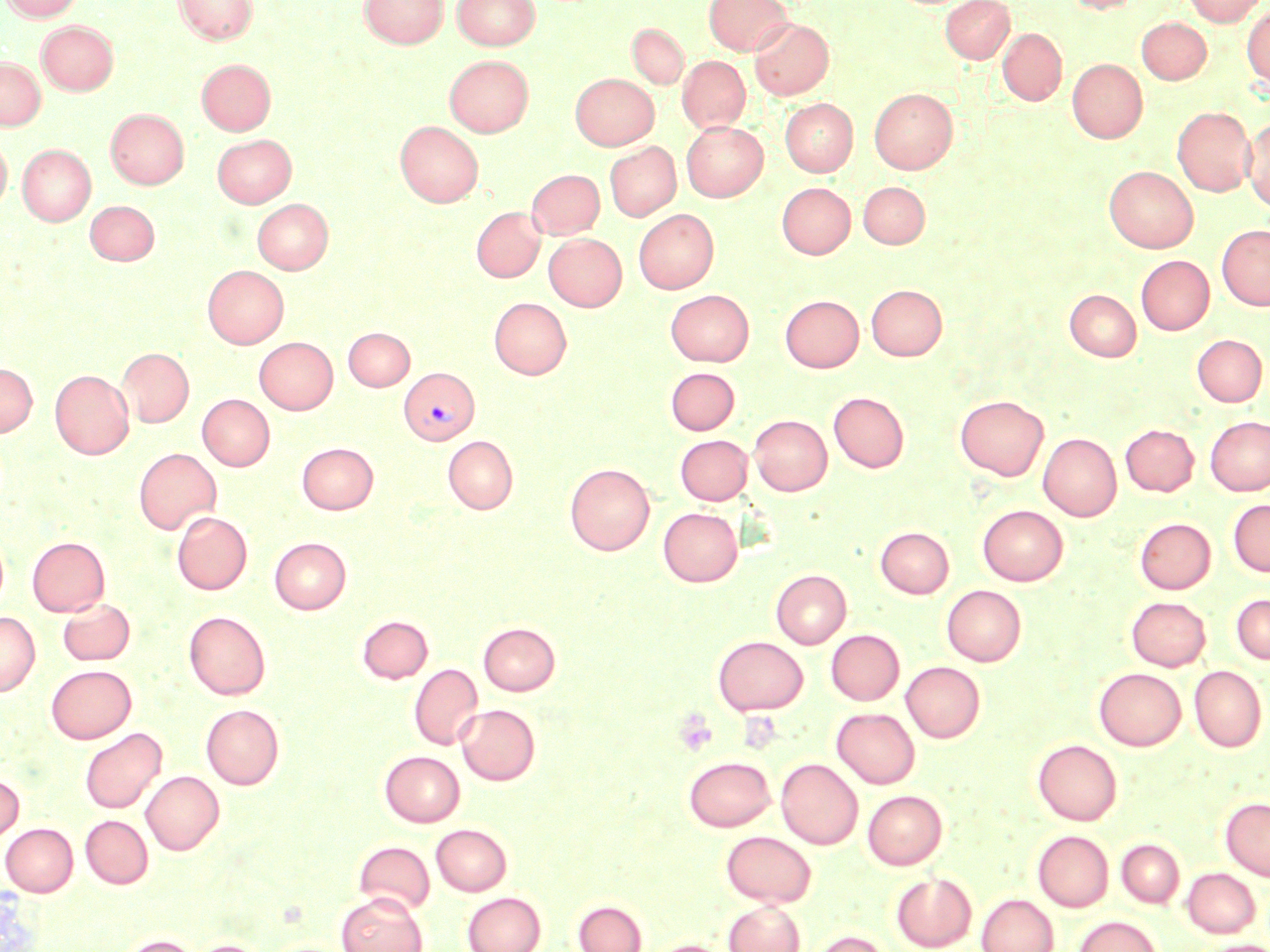

Summary:
  - Coordinate format: approximate bounding boxes as [x1, y1, x2, y2] in pixels
  - Uninfected red blood cell locations: [1, 0, 85, 21], [174, 0, 257, 45], [360, 0, 448, 48], [452, 0, 540, 51], [704, 0, 793, 56], [941, 0, 1014, 63], [1064, 0, 1141, 14], [1184, 0, 1266, 26], [1209, 3, 1264, 42], [1242, 5, 1270, 90], [1137, 17, 1212, 83], [750, 19, 833, 99], [37, 21, 119, 94], [628, 24, 688, 88], [997, 28, 1066, 105], [445, 55, 533, 137], [678, 56, 750, 133], [0, 57, 45, 130], [197, 59, 275, 135], [1067, 59, 1148, 143], [570, 73, 658, 150], [869, 88, 957, 174], [781, 98, 857, 176], [1172, 106, 1255, 196], [106, 108, 188, 189], [1243, 116, 1270, 211], [395, 120, 483, 207], [682, 122, 767, 201], [212, 134, 296, 207], [0, 136, 12, 213], [605, 142, 680, 221], [17, 143, 96, 225], [1104, 165, 1199, 252], [527, 169, 604, 238], [777, 182, 855, 258], [859, 182, 929, 248], [253, 199, 332, 273], [85, 200, 159, 265], [471, 207, 545, 282], [634, 209, 718, 293], [1217, 224, 1270, 310], [544, 233, 626, 310], [1136, 255, 1213, 334], [203, 265, 288, 348], [867, 284, 947, 360], [1065, 289, 1141, 361], [666, 290, 754, 366], [780, 295, 863, 372], [489, 297, 571, 379], [343, 327, 414, 391], [1192, 334, 1267, 406], [254, 337, 337, 414], [118, 348, 194, 427], [0, 363, 37, 436], [666, 367, 739, 435], [50, 370, 133, 459], [829, 391, 908, 472], [197, 394, 274, 470], [955, 394, 1048, 480], [749, 414, 832, 495], [1205, 416, 1270, 495], [1120, 424, 1198, 496], [1039, 433, 1121, 520], [675, 434, 752, 505], [443, 435, 518, 513], [297, 442, 378, 514], [134, 448, 221, 534], [565, 463, 655, 555], [1228, 499, 1270, 576], [978, 505, 1067, 585], [658, 508, 743, 586], [172, 511, 252, 594], [1135, 518, 1215, 593], [876, 527, 953, 597], [27, 536, 109, 616], [270, 537, 350, 613], [771, 569, 851, 648], [942, 585, 1026, 666], [1231, 593, 1270, 664], [1126, 595, 1211, 671], [57, 598, 135, 666], [184, 610, 270, 699], [0, 612, 40, 696], [358, 615, 432, 683], [479, 623, 560, 695], [826, 629, 904, 705], [713, 635, 808, 714], [901, 661, 985, 742], [409, 664, 483, 750], [46, 665, 136, 743], [1189, 665, 1266, 751], [1094, 667, 1185, 750], [201, 704, 284, 789], [456, 704, 540, 785], [832, 708, 919, 788], [80, 727, 166, 813], [1033, 739, 1122, 825], [380, 750, 464, 826], [683, 755, 776, 832], [776, 758, 862, 849], [141, 770, 224, 854], [0, 774, 24, 843], [862, 790, 947, 869], [1221, 797, 1270, 880], [81, 815, 152, 888], [1, 823, 77, 896], [431, 824, 511, 895], [722, 830, 816, 906], [1033, 830, 1114, 912], [1117, 839, 1184, 907], [354, 840, 435, 914], [1182, 867, 1260, 937], [891, 872, 976, 951], [463, 891, 545, 952], [337, 892, 427, 952], [976, 894, 1058, 952], [573, 899, 647, 952], [724, 900, 805, 952], [1074, 915, 1162, 952], [810, 931, 891, 952], [120, 935, 198, 952], [188, 939, 267, 952], [650, 940, 730, 952], [1201, 940, 1270, 952]
  - Platelet locations: [674, 709, 717, 756]
  - Plasmodium vivax-infected red blood cell locations: [399, 366, 479, 444]
  - Slide-level diagnosis: Plasmodium vivax
  - Modality: light microscopy
  - Stain: May-Grünwald-Giemsa
  - Magnification: 1000x
  - Field of view: one of a larger specimen
  - Image size: 1270×952 pixels
  - Preparation: thin blood smear